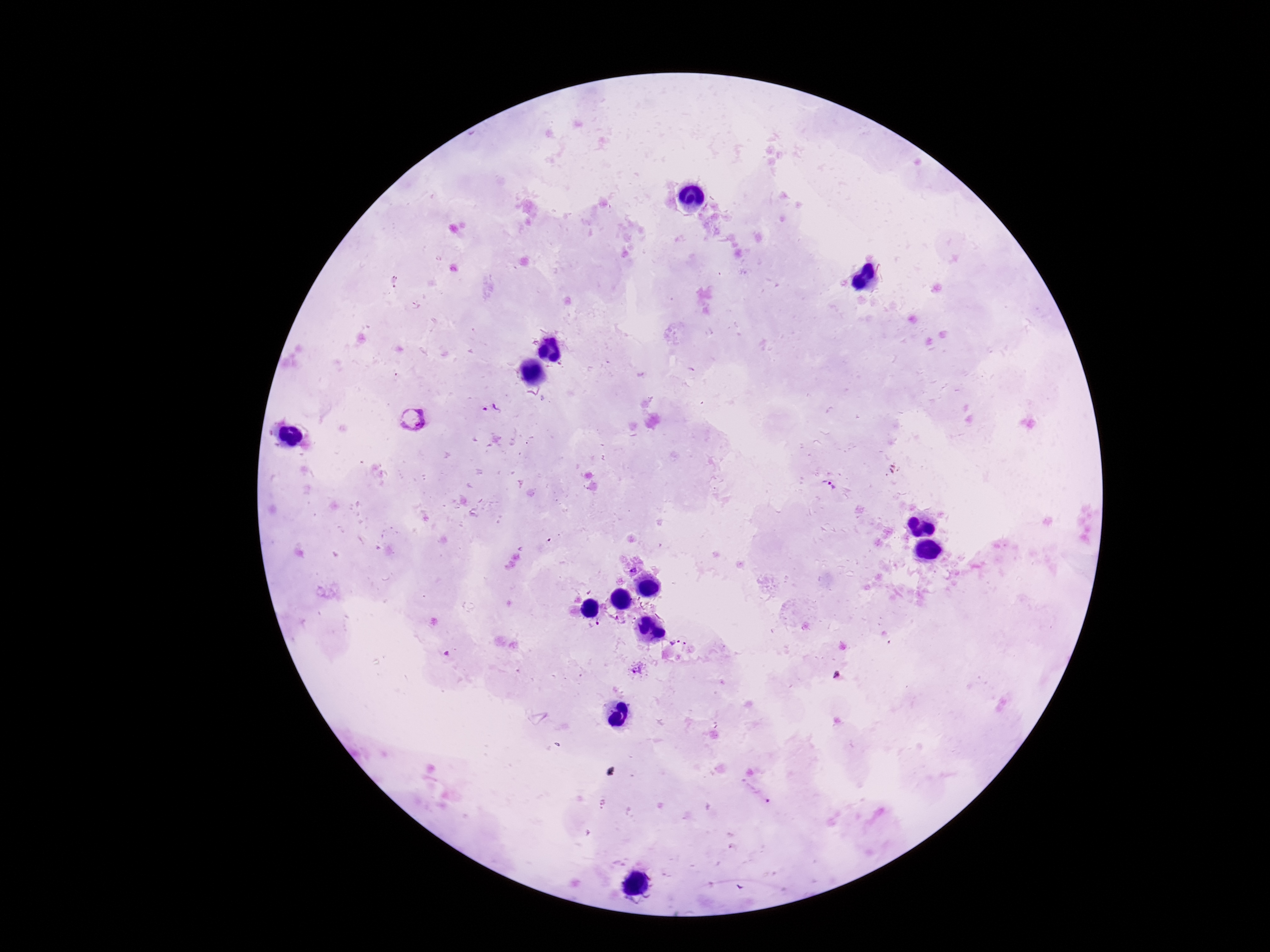
field of view = single
stain = Giemsa
capture = smartphone camera through the microscope eyepiece
Plasmodium parasite locations = approximate centers as [x, y] in pixels: [490, 407], [412, 419], [828, 484], [632, 569], [676, 642], [686, 646], [637, 670]
image size = 1270×952 pixels
magnification = 100x
preparation = thick blood film
patient malaria status = positive